Describe the morphology of the erythrocytes.
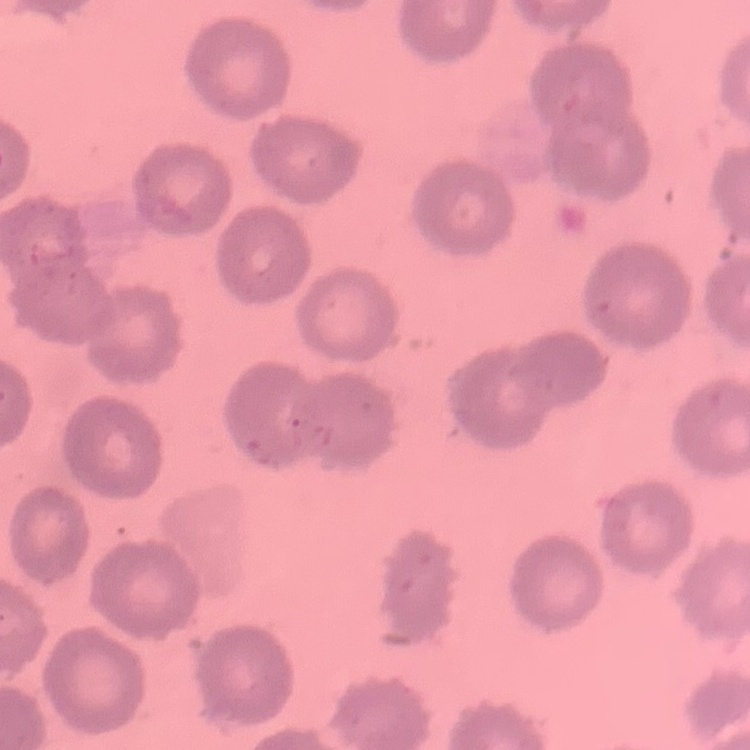
They show no rouleaux formation.

Square crop of a larger photomicrograph. Thin blood film. Stained with either Field's or Giemsa.